Give the preparation type.
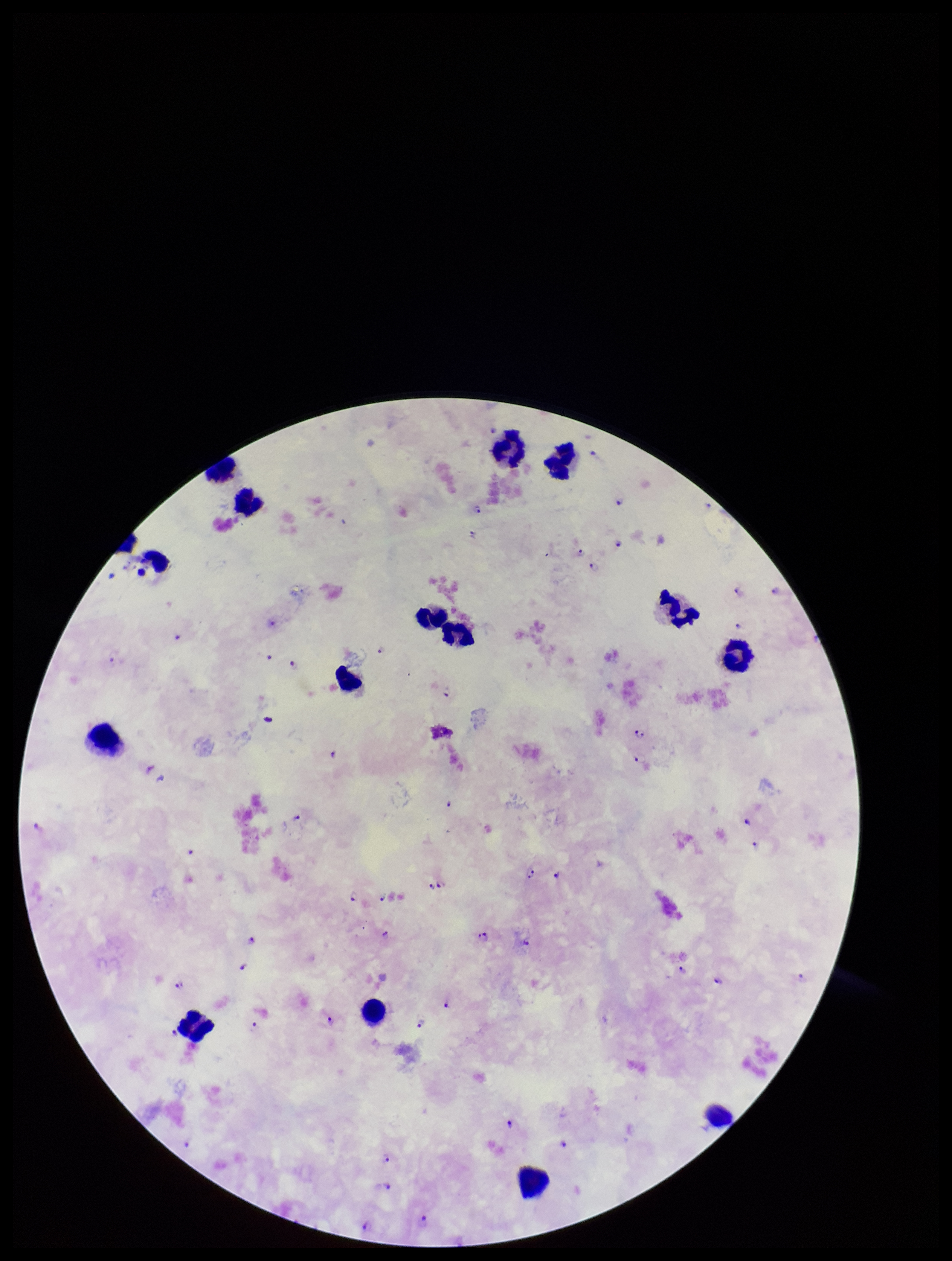

Thick.

Giemsa stain. Parasite count: 49. Photographed through the microscope eyepiece with a smartphone camera. Patient malaria status: positive. Image is 952×1261 pixels. Leukocyte count: 14. Species reported for this patient: Plasmodium falciparum. Plasmodium parasites: detected. Single field of view.